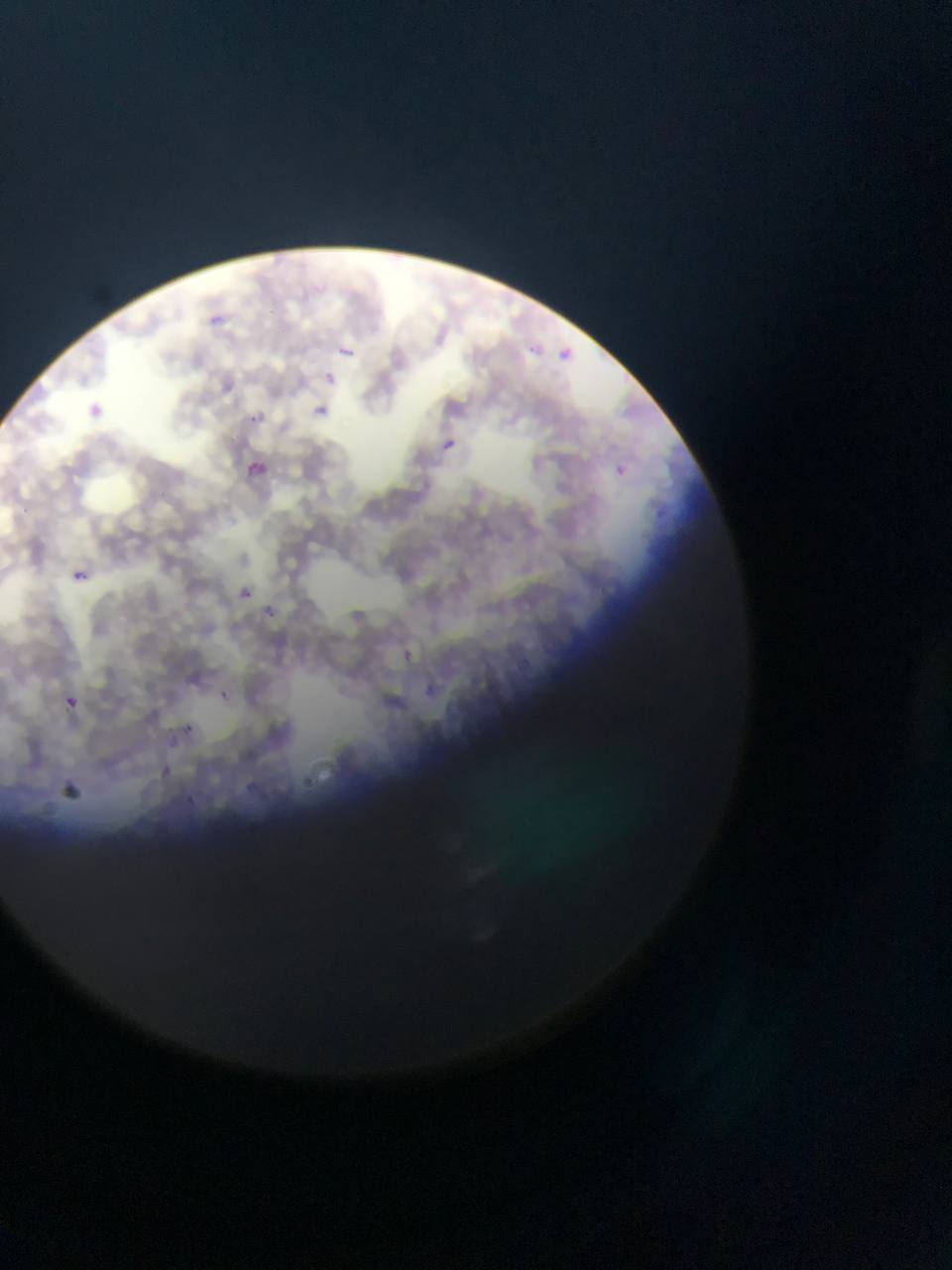

Approximate bounding boxes as left top right bottom in pixels. Plasmodium parasite locations: 210 311 235 331; 331 343 360 360; 563 344 575 361; 317 368 340 390; 311 402 334 422; 245 411 266 429; 440 438 456 453; 241 456 272 483; 606 463 631 485; 71 569 88 584; 233 584 256 605; 265 599 283 622; 389 643 421 672; 219 688 233 700; 423 689 442 703; 61 693 81 713; 185 721 201 735; 165 765 180 782; 303 779 318 792. Thin blood smear. Image is 952×1270 pixels. Photographed through a microscope with a mobile-phone camera. Single field of view. Sample from Ghana.